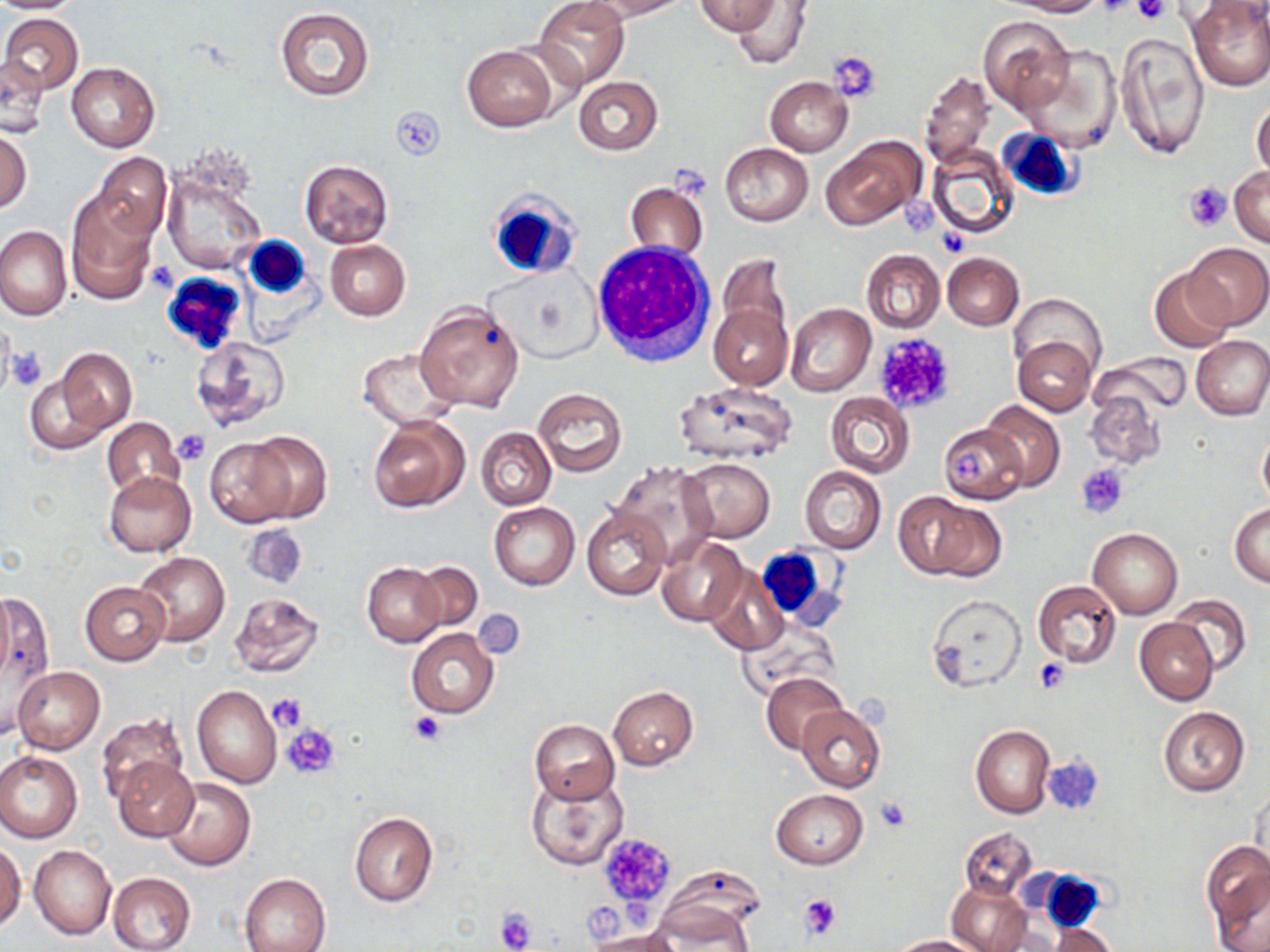
Approximate bounding boxes as named x1/y1/x2/y2 corners in pixels. White blood cell locations: (x1=995, y1=128, x2=1080, y2=201), (x1=485, y1=188, x2=582, y2=282), (x1=243, y1=236, x2=310, y2=297), (x1=593, y1=245, x2=717, y2=369), (x1=161, y1=271, x2=247, y2=355), (x1=758, y1=543, x2=852, y2=630), (x1=1034, y1=870, x2=1106, y2=932). Uninfected red blood cell locations: (x1=0, y1=0, x2=84, y2=13), (x1=534, y1=0, x2=629, y2=88), (x1=588, y1=0, x2=690, y2=21), (x1=730, y1=0, x2=812, y2=68), (x1=1002, y1=0, x2=1103, y2=16), (x1=1187, y1=0, x2=1270, y2=92), (x1=694, y1=1, x2=780, y2=35), (x1=1193, y1=3, x2=1270, y2=28), (x1=275, y1=6, x2=374, y2=101), (x1=1, y1=12, x2=84, y2=93), (x1=978, y1=15, x2=1074, y2=115), (x1=1115, y1=33, x2=1209, y2=159), (x1=462, y1=46, x2=557, y2=131), (x1=1019, y1=46, x2=1122, y2=153), (x1=1, y1=56, x2=49, y2=137), (x1=66, y1=62, x2=160, y2=152), (x1=919, y1=71, x2=995, y2=171), (x1=573, y1=77, x2=663, y2=155), (x1=764, y1=77, x2=853, y2=156), (x1=1251, y1=99, x2=1270, y2=181), (x1=0, y1=125, x2=32, y2=214), (x1=821, y1=134, x2=923, y2=230), (x1=720, y1=143, x2=813, y2=227), (x1=926, y1=144, x2=1021, y2=240), (x1=92, y1=151, x2=172, y2=241), (x1=300, y1=159, x2=393, y2=247), (x1=1230, y1=166, x2=1270, y2=246), (x1=162, y1=168, x2=266, y2=276), (x1=625, y1=181, x2=711, y2=262), (x1=64, y1=192, x2=159, y2=306), (x1=0, y1=226, x2=72, y2=321), (x1=326, y1=240, x2=411, y2=320), (x1=1186, y1=242, x2=1269, y2=329), (x1=861, y1=249, x2=944, y2=334), (x1=943, y1=253, x2=1024, y2=330), (x1=716, y1=255, x2=795, y2=359), (x1=1149, y1=267, x2=1238, y2=352), (x1=1011, y1=293, x2=1106, y2=378), (x1=709, y1=299, x2=791, y2=391), (x1=415, y1=302, x2=525, y2=413), (x1=786, y1=303, x2=876, y2=397), (x1=189, y1=335, x2=291, y2=433), (x1=1191, y1=335, x2=1270, y2=420), (x1=1013, y1=336, x2=1095, y2=417), (x1=44, y1=348, x2=139, y2=444), (x1=358, y1=349, x2=459, y2=430), (x1=1095, y1=351, x2=1193, y2=417), (x1=673, y1=381, x2=798, y2=466), (x1=532, y1=389, x2=628, y2=477), (x1=1084, y1=389, x2=1165, y2=471), (x1=824, y1=392, x2=914, y2=477), (x1=980, y1=402, x2=1065, y2=492), (x1=102, y1=417, x2=185, y2=500), (x1=368, y1=417, x2=470, y2=513), (x1=939, y1=424, x2=1026, y2=505), (x1=476, y1=427, x2=557, y2=509), (x1=1257, y1=430, x2=1270, y2=511), (x1=244, y1=431, x2=333, y2=522), (x1=205, y1=435, x2=301, y2=527), (x1=679, y1=458, x2=775, y2=542), (x1=612, y1=462, x2=719, y2=565), (x1=799, y1=465, x2=886, y2=554), (x1=103, y1=470, x2=198, y2=557), (x1=893, y1=491, x2=996, y2=580), (x1=488, y1=501, x2=580, y2=590), (x1=1229, y1=502, x2=1270, y2=587), (x1=582, y1=506, x2=670, y2=601), (x1=1089, y1=528, x2=1183, y2=619), (x1=656, y1=536, x2=748, y2=628), (x1=134, y1=551, x2=229, y2=646), (x1=362, y1=561, x2=445, y2=647), (x1=411, y1=562, x2=482, y2=632), (x1=704, y1=568, x2=788, y2=655), (x1=1032, y1=580, x2=1121, y2=669), (x1=79, y1=582, x2=170, y2=666), (x1=0, y1=585, x2=54, y2=725), (x1=228, y1=592, x2=325, y2=677), (x1=927, y1=593, x2=1026, y2=692), (x1=1169, y1=593, x2=1253, y2=677), (x1=1135, y1=618, x2=1219, y2=705), (x1=736, y1=619, x2=840, y2=700), (x1=406, y1=626, x2=500, y2=719), (x1=12, y1=666, x2=106, y2=754), (x1=761, y1=671, x2=848, y2=754), (x1=192, y1=685, x2=282, y2=788), (x1=608, y1=685, x2=698, y2=770), (x1=796, y1=705, x2=886, y2=792), (x1=1158, y1=707, x2=1250, y2=796), (x1=95, y1=714, x2=188, y2=805), (x1=530, y1=719, x2=620, y2=804), (x1=971, y1=725, x2=1055, y2=818), (x1=0, y1=751, x2=83, y2=842), (x1=112, y1=759, x2=198, y2=842), (x1=527, y1=773, x2=629, y2=870), (x1=162, y1=778, x2=255, y2=871), (x1=1250, y1=782, x2=1269, y2=871), (x1=772, y1=790, x2=868, y2=869), (x1=349, y1=812, x2=438, y2=906), (x1=960, y1=827, x2=1038, y2=901), (x1=1202, y1=841, x2=1269, y2=940), (x1=0, y1=842, x2=25, y2=930), (x1=29, y1=844, x2=116, y2=940), (x1=107, y1=872, x2=197, y2=952), (x1=240, y1=873, x2=331, y2=952), (x1=647, y1=878, x2=762, y2=951), (x1=947, y1=878, x2=1030, y2=952), (x1=1048, y1=922, x2=1119, y2=951), (x1=588, y1=929, x2=683, y2=952), (x1=888, y1=935, x2=979, y2=951). Platelet locations: (x1=1131, y1=0, x2=1170, y2=23), (x1=1097, y1=1, x2=1139, y2=20), (x1=829, y1=52, x2=882, y2=104), (x1=392, y1=107, x2=446, y2=160), (x1=670, y1=163, x2=706, y2=202), (x1=1185, y1=182, x2=1230, y2=231), (x1=901, y1=195, x2=936, y2=236), (x1=872, y1=334, x2=955, y2=415), (x1=5, y1=346, x2=48, y2=390), (x1=173, y1=429, x2=212, y2=466), (x1=956, y1=449, x2=984, y2=485), (x1=1074, y1=462, x2=1128, y2=518), (x1=1034, y1=659, x2=1069, y2=695), (x1=268, y1=692, x2=309, y2=730), (x1=408, y1=709, x2=448, y2=746), (x1=284, y1=723, x2=340, y2=779), (x1=1043, y1=754, x2=1105, y2=815), (x1=875, y1=796, x2=911, y2=833), (x1=598, y1=832, x2=676, y2=910), (x1=799, y1=892, x2=844, y2=941), (x1=495, y1=908, x2=536, y2=952). Slide-level diagnosis: negative for blood parasites. Image is 1270×952 pixels. Thin blood film. One field of a larger specimen. 1000x magnification. Light microscopy. May-Grünwald-Giemsa stain.